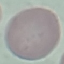

Summary:
  - Result: negative for malaria parasites
  - Stain: Giemsa
  - Image type: cell patch, automatically extracted from a larger field of view and resized to 64 × 64 pixels
  - Capture: smartphone camera at the microscope eyepiece
  - Preparation: thin blood film